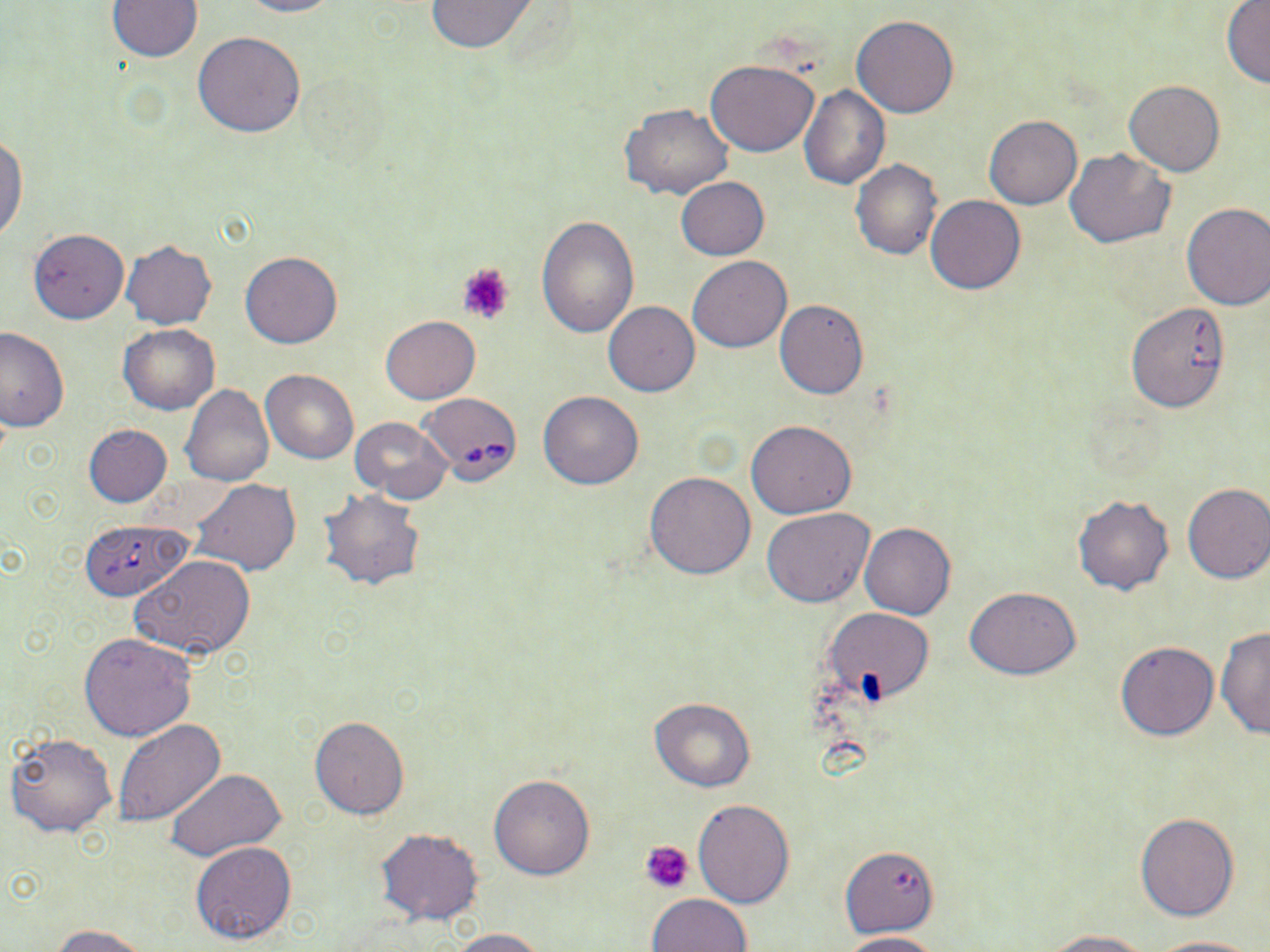

Summary:
  - Coordinate format: approximate bounding boxes as (x1,y1)-(x2,y2) corner pairs in pixels
  - Uninfected red blood cell locations: (236,0)-(344,18), (423,0)-(541,52), (106,1)-(202,61), (1221,2)-(1270,88), (852,14)-(961,118), (193,31)-(306,137), (705,60)-(820,156), (1125,81)-(1224,175), (799,85)-(891,189), (620,104)-(731,200), (984,115)-(1082,209), (0,133)-(28,244), (1064,148)-(1176,248), (851,161)-(942,260), (675,177)-(769,260), (926,194)-(1025,295), (1181,202)-(1270,310), (536,214)-(640,339), (28,228)-(129,323), (121,240)-(217,328), (240,251)-(342,348), (688,256)-(791,352), (1127,298)-(1228,415), (774,299)-(869,400), (603,301)-(700,396), (380,316)-(481,404), (119,325)-(220,414), (0,326)-(68,432), (261,370)-(359,464), (182,385)-(274,486), (538,391)-(644,489), (349,416)-(452,503), (747,419)-(856,518), (83,424)-(172,506), (645,471)-(755,580), (192,479)-(300,576), (1182,482)-(1270,584), (318,488)-(425,591), (1072,493)-(1175,596), (762,508)-(875,608), (859,522)-(956,620), (131,554)-(258,660), (965,586)-(1081,678), (823,608)-(933,702), (1217,626)-(1270,739), (79,633)-(195,741), (1114,641)-(1219,741), (649,697)-(755,791), (310,716)-(409,818), (113,719)-(225,826), (4,732)-(116,838), (165,768)-(287,863), (489,773)-(595,880), (693,800)-(794,907), (1135,812)-(1239,922), (376,828)-(487,927), (191,841)-(296,945), (840,845)-(938,937), (647,894)-(752,952), (51,924)-(150,952), (447,927)-(552,951), (1042,929)-(1156,951), (841,931)-(946,952), (1146,936)-(1258,952)
  - Platelet locations: (457,262)-(514,325), (641,840)-(694,894)
  - Babesia divergens-infected red blood cell locations: (418,391)-(524,484), (80,520)-(191,602)
  - Slide-level diagnosis: Babesia divergens
  - Field of view: single
  - Stain: May-Grünwald-Giemsa
  - Image size: 1270×952 pixels
  - Preparation: thin blood smear
  - Modality: optical microscopy
  - Magnification: 1000x